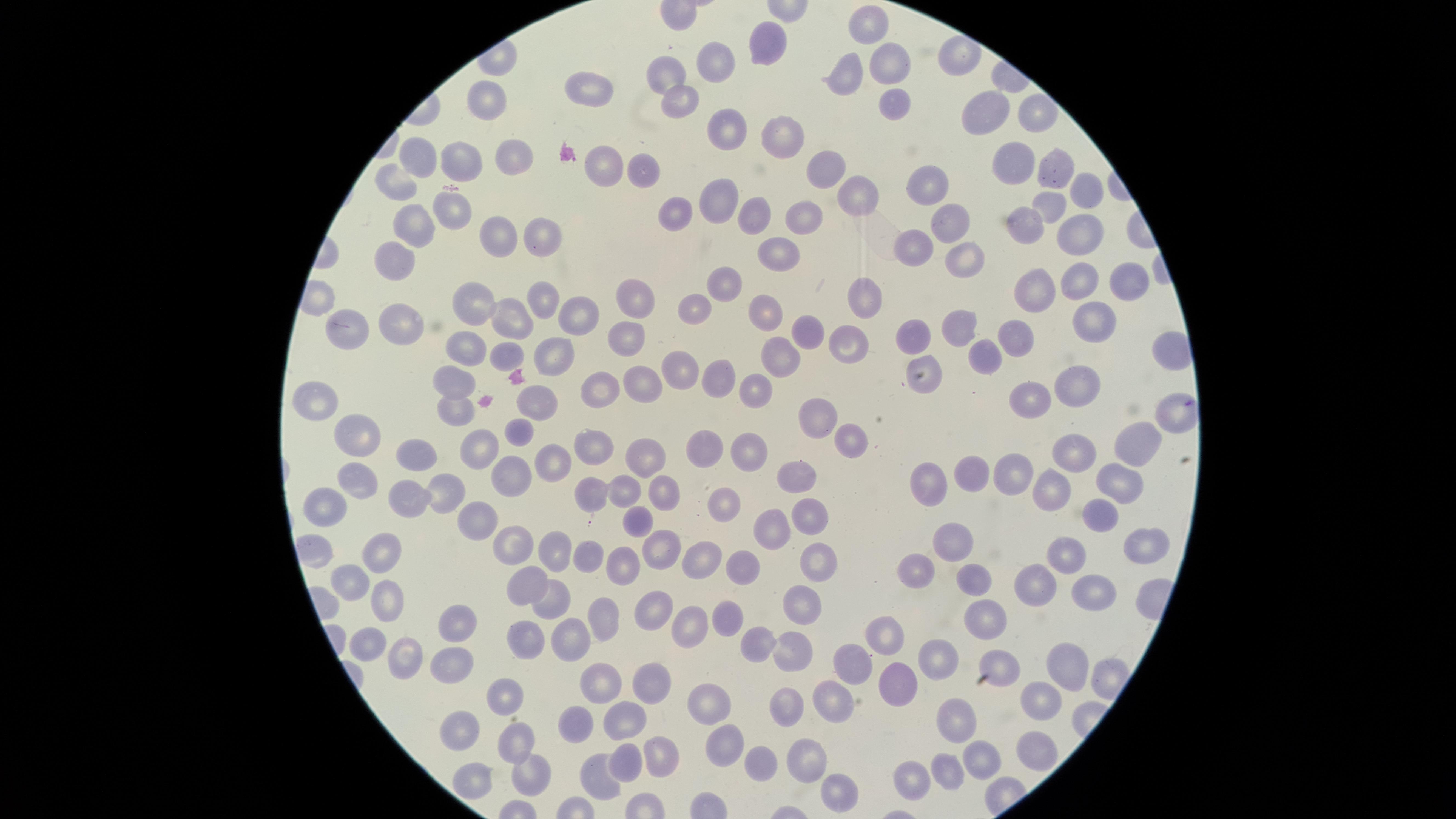

{
  "presence": "no malaria parasites detected",
  "visible_region": "circular",
  "image_size": "1456×819 pixels",
  "preparation": "thin smear of blood",
  "uninfected_RBCs": "approximate marker points, in pixels from the top-left corner: (x=875, y=27), (x=767, y=41), (x=719, y=64), (x=893, y=68), (x=665, y=73), (x=851, y=75), (x=595, y=84), (x=895, y=99), (x=677, y=100), (x=487, y=103), (x=983, y=110), (x=1031, y=113), (x=720, y=123), (x=775, y=135), (x=420, y=158), (x=512, y=159), (x=455, y=162), (x=1002, y=163), (x=605, y=165), (x=1052, y=167), (x=643, y=168), (x=829, y=179), (x=931, y=182), (x=394, y=185), (x=1077, y=187), (x=717, y=194), (x=857, y=194), (x=1049, y=205), (x=451, y=208), (x=680, y=213), (x=751, y=214), (x=803, y=217), (x=950, y=222), (x=420, y=223), (x=1023, y=228), (x=498, y=232), (x=1072, y=232), (x=529, y=233), (x=783, y=248), (x=911, y=252), (x=961, y=257), (x=391, y=261), (x=1120, y=279), (x=1078, y=280), (x=727, y=282), (x=1038, y=288), (x=630, y=294), (x=548, y=297), (x=860, y=297), (x=475, y=303), (x=698, y=307), (x=765, y=310), (x=574, y=317), (x=1091, y=320), (x=515, y=322), (x=356, y=323), (x=400, y=323), (x=955, y=327), (x=803, y=332), (x=911, y=336), (x=1018, y=339), (x=626, y=340), (x=845, y=341), (x=467, y=346), (x=555, y=350), (x=507, y=351), (x=783, y=356), (x=976, y=357), (x=925, y=368), (x=681, y=369), (x=454, y=376), (x=719, y=376), (x=1073, y=384), (x=607, y=385), (x=642, y=385), (x=759, y=386), (x=531, y=396), (x=1042, y=398), (x=312, y=400), (x=455, y=412), (x=822, y=420), (x=518, y=425), (x=351, y=431), (x=857, y=438), (x=1122, y=443), (x=583, y=444), (x=483, y=446), (x=413, y=447), (x=703, y=447), (x=1068, y=448), (x=744, y=449), (x=636, y=455), (x=547, y=461), (x=791, y=474), (x=964, y=474), (x=511, y=475), (x=1010, y=478), (x=932, y=479), (x=359, y=480), (x=1120, y=480), (x=1050, y=492), (x=618, y=494), (x=591, y=495), (x=447, y=498), (x=662, y=498), (x=407, y=502), (x=724, y=505), (x=325, y=506), (x=1095, y=515), (x=474, y=516), (x=630, y=522), (x=816, y=522), (x=769, y=528), (x=1138, y=544), (x=386, y=545), (x=945, y=546), (x=659, y=548), (x=1063, y=548), (x=510, y=553), (x=551, y=555), (x=587, y=560), (x=620, y=562), (x=913, y=562), (x=705, y=564), (x=741, y=566), (x=818, y=566), (x=974, y=575), (x=1034, y=579), (x=351, y=581), (x=526, y=584), (x=1089, y=587), (x=384, y=595), (x=797, y=598), (x=552, y=604), (x=657, y=611), (x=990, y=617), (x=601, y=618), (x=726, y=621), (x=686, y=626), (x=457, y=629), (x=573, y=634), (x=523, y=635), (x=751, y=640), (x=887, y=640), (x=365, y=641), (x=400, y=654), (x=787, y=656), (x=937, y=657), (x=857, y=663), (x=1068, y=663), (x=453, y=668), (x=1004, y=671), (x=602, y=680), (x=651, y=682), (x=898, y=685), (x=504, y=694), (x=1044, y=700), (x=790, y=701), (x=708, y=702), (x=831, y=703), (x=577, y=720), (x=620, y=720), (x=956, y=724), (x=463, y=732), (x=517, y=739), (x=719, y=744), (x=1030, y=746), (x=661, y=751), (x=760, y=760), (x=625, y=761), (x=980, y=761), (x=813, y=764), (x=531, y=767), (x=469, y=774), (x=946, y=774), (x=592, y=777), (x=909, y=779), (x=828, y=798)",
  "capture": "smartphone photograph through the microscope eyepiece",
  "field_of_view": "single",
  "stain": "Giemsa"
}